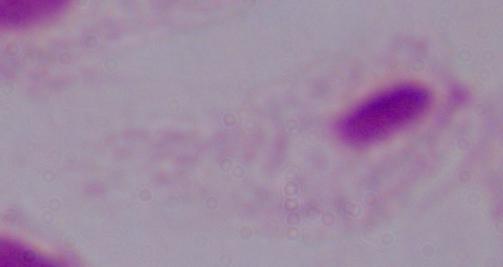
Summary:
  - Identification: trichomonad
  - Modality: photomicrograph
  - Magnification: 1000x